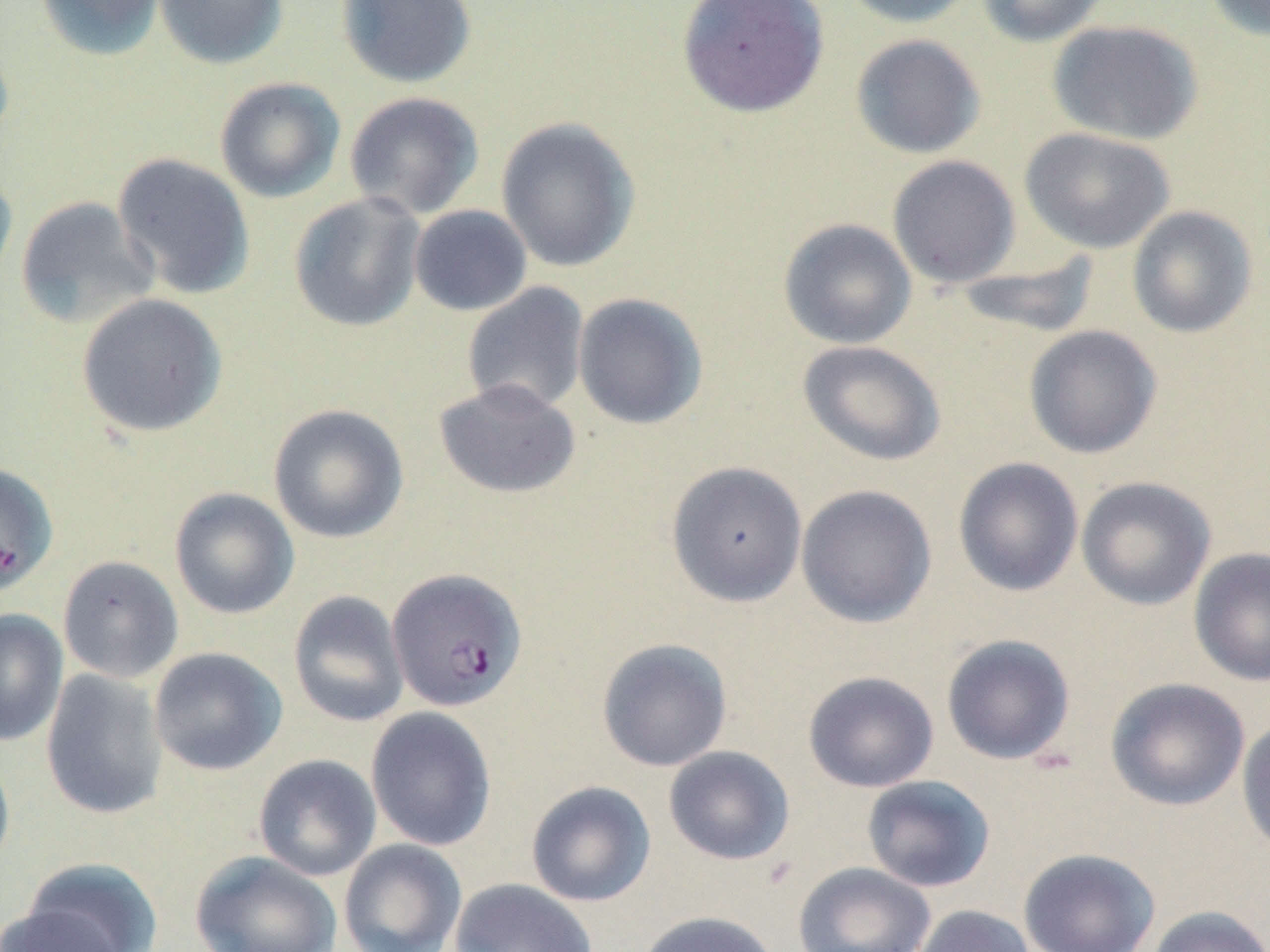

Approximate bounding boxes as named x1/y1/x2/y2 corners in pixels. Plasmodium falciparum-infected red blood cell locations (subset): (x1=386, y1=568, x2=527, y2=711). Uninfected red blood cell locations (subset): (x1=34, y1=0, x2=166, y2=62), (x1=154, y1=0, x2=290, y2=70), (x1=335, y1=0, x2=477, y2=89), (x1=676, y1=0, x2=830, y2=118), (x1=839, y1=0, x2=979, y2=28), (x1=976, y1=0, x2=1112, y2=47), (x1=1201, y1=0, x2=1270, y2=41), (x1=1047, y1=19, x2=1203, y2=145), (x1=849, y1=34, x2=986, y2=159), (x1=214, y1=77, x2=346, y2=203), (x1=343, y1=91, x2=484, y2=220), (x1=495, y1=116, x2=641, y2=273), (x1=1019, y1=127, x2=1175, y2=254), (x1=112, y1=152, x2=256, y2=300), (x1=887, y1=155, x2=1021, y2=288), (x1=0, y1=165, x2=18, y2=298), (x1=289, y1=192, x2=426, y2=333), (x1=15, y1=196, x2=158, y2=328), (x1=408, y1=205, x2=533, y2=316), (x1=1126, y1=205, x2=1258, y2=338), (x1=778, y1=218, x2=917, y2=349), (x1=951, y1=251, x2=1102, y2=341), (x1=461, y1=282, x2=590, y2=416), (x1=75, y1=293, x2=228, y2=438), (x1=572, y1=293, x2=708, y2=430), (x1=1023, y1=325, x2=1162, y2=459), (x1=797, y1=339, x2=947, y2=466), (x1=433, y1=379, x2=581, y2=500), (x1=268, y1=403, x2=409, y2=544), (x1=953, y1=457, x2=1084, y2=597), (x1=665, y1=461, x2=808, y2=607), (x1=1076, y1=476, x2=1216, y2=611), (x1=795, y1=484, x2=937, y2=627), (x1=169, y1=487, x2=300, y2=619), (x1=1189, y1=547, x2=1270, y2=687), (x1=58, y1=555, x2=184, y2=683), (x1=288, y1=590, x2=409, y2=727), (x1=0, y1=609, x2=67, y2=747), (x1=941, y1=634, x2=1076, y2=765), (x1=596, y1=638, x2=733, y2=771), (x1=149, y1=647, x2=287, y2=776), (x1=40, y1=668, x2=169, y2=820), (x1=802, y1=671, x2=939, y2=793), (x1=1105, y1=677, x2=1250, y2=811), (x1=366, y1=706, x2=497, y2=852), (x1=1236, y1=717, x2=1270, y2=858), (x1=663, y1=746, x2=795, y2=865), (x1=0, y1=747, x2=15, y2=877), (x1=253, y1=754, x2=381, y2=881), (x1=861, y1=775, x2=995, y2=893), (x1=525, y1=780, x2=657, y2=907), (x1=338, y1=839, x2=467, y2=952), (x1=1018, y1=847, x2=1161, y2=952), (x1=189, y1=850, x2=342, y2=952), (x1=17, y1=858, x2=165, y2=952), (x1=792, y1=862, x2=935, y2=952), (x1=449, y1=878, x2=598, y2=952), (x1=1, y1=901, x2=128, y2=952), (x1=912, y1=904, x2=1036, y2=952), (x1=1146, y1=904, x2=1270, y2=952), (x1=634, y1=910, x2=781, y2=952). Slide-level diagnosis: Plasmodium falciparum. Thin blood film. May-Grünwald-Giemsa stain. Light microscopy. Image is 1270×952 pixels. 1000x magnification. Single field of view.